Classify this cell by malaria status.
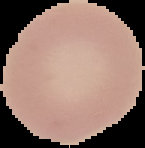
Uninfected.

Summary:
  - Image type: segmented cell region with the area outside set to black
  - Image size: 145×148 pixels
  - Preparation: thin blood smear